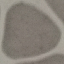
Summary:
  - Result: no malaria parasites detected
  - Preparation: thin blood smear
  - Capture: smartphone camera at the microscope eyepiece
  - Stain: Giemsa
  - Image type: automatically extracted cell patch, resized to 64 × 64 pixels